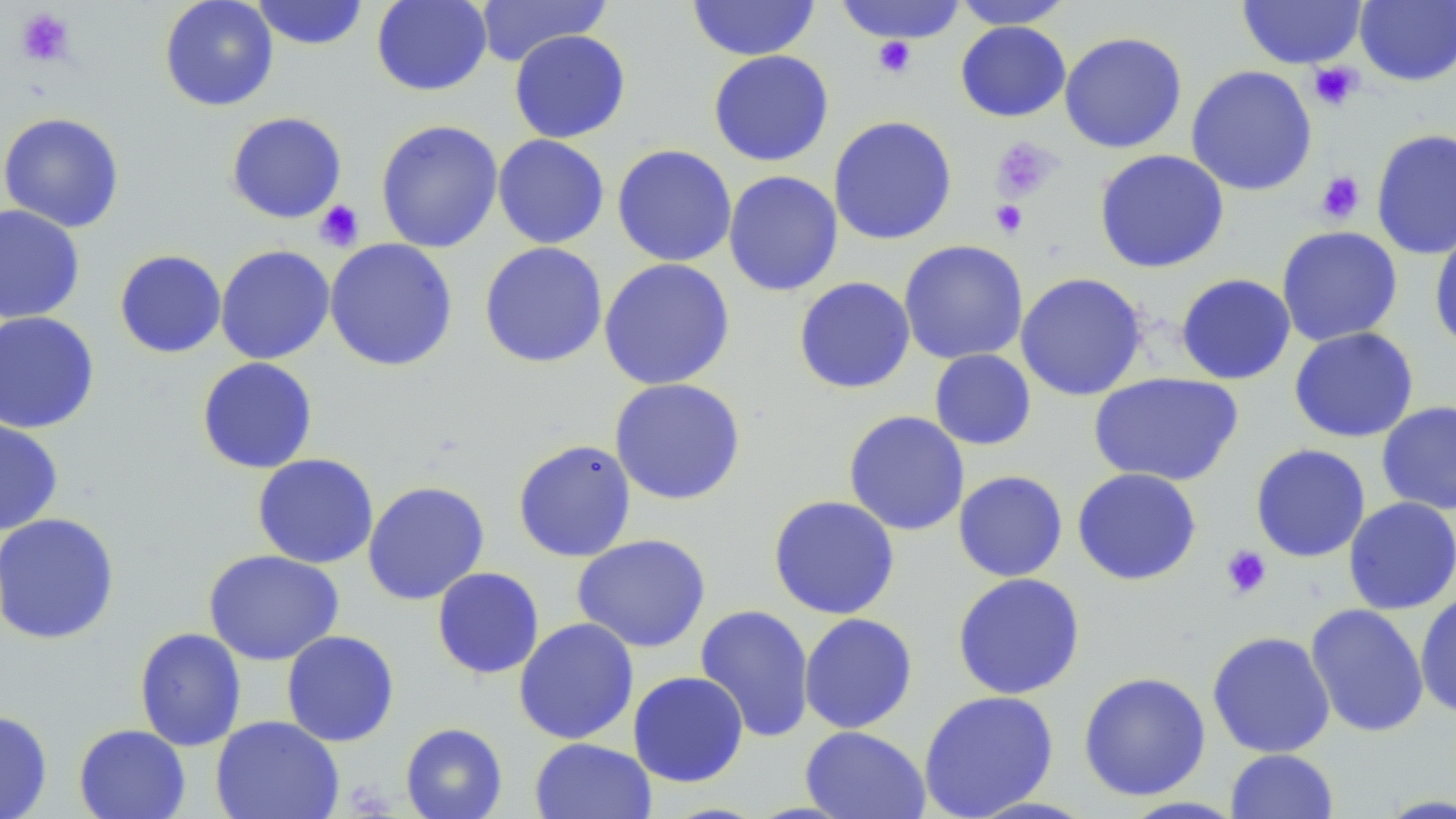 Approximate bounding boxes as [x1, y1, x2, y2] in pixels. Uninfected red blood cell locations: [159, 0, 279, 112], [249, 0, 370, 50], [371, 0, 492, 96], [473, 0, 612, 67], [685, 0, 821, 61], [834, 0, 971, 44], [950, 0, 1076, 30], [1236, 0, 1368, 69], [1354, 0, 1456, 86], [954, 20, 1071, 122], [508, 29, 631, 143], [1059, 31, 1188, 154], [707, 49, 834, 167], [1185, 65, 1318, 197], [225, 111, 347, 224], [0, 112, 125, 232], [828, 115, 958, 245], [375, 119, 503, 253], [1371, 128, 1456, 260], [492, 134, 610, 249], [611, 144, 737, 267], [1093, 149, 1230, 274], [722, 170, 843, 296], [0, 204, 85, 324], [1429, 222, 1456, 352], [1276, 225, 1404, 347], [324, 238, 458, 372], [898, 239, 1029, 365], [479, 241, 608, 368], [215, 244, 336, 365], [114, 249, 227, 358], [598, 258, 736, 391], [1015, 272, 1148, 401], [1175, 273, 1296, 385], [793, 276, 916, 394], [0, 311, 101, 434], [1288, 326, 1419, 443], [929, 349, 1037, 451], [196, 357, 318, 474], [1088, 373, 1244, 486], [609, 377, 746, 506], [1376, 401, 1456, 516], [843, 410, 970, 536], [0, 417, 63, 535], [512, 439, 637, 562], [1250, 443, 1371, 563], [252, 453, 379, 569], [1072, 467, 1202, 586], [953, 470, 1068, 583], [362, 480, 490, 605], [767, 494, 901, 620], [1343, 497, 1456, 615], [0, 512, 121, 645], [571, 534, 711, 653], [203, 549, 344, 666], [431, 567, 544, 679], [952, 572, 1086, 700], [1415, 591, 1456, 721], [1305, 603, 1429, 737], [695, 604, 815, 743], [798, 612, 918, 734], [513, 617, 639, 745], [134, 627, 247, 751], [281, 630, 400, 747], [1207, 631, 1336, 758], [627, 671, 749, 787], [1078, 671, 1211, 801], [918, 690, 1059, 818], [0, 710, 53, 819], [210, 714, 344, 819], [400, 722, 508, 819], [73, 723, 191, 819], [799, 725, 931, 818], [529, 738, 656, 819], [1225, 748, 1338, 819]. Platelet locations: [15, 7, 76, 67], [873, 37, 917, 78], [1308, 61, 1364, 111], [992, 137, 1060, 202], [1315, 172, 1366, 223], [314, 199, 365, 252], [989, 199, 1029, 238], [1220, 545, 1272, 599]. Slide-level diagnosis: negative for blood parasites. Thin blood smear. Captured at 1000x magnification. Optical microscopy. Single field of view. May-Grünwald-Giemsa stain. Image is 1456×819 pixels.